Report the malaria status of this cell.
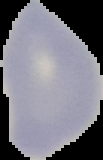

It is uninfected.

Summary:
  - Preparation: thin blood smear
  - Image type: segmented cell region with the area outside set to black
  - Image size: 103×160 pixels